Identify the preparation type.
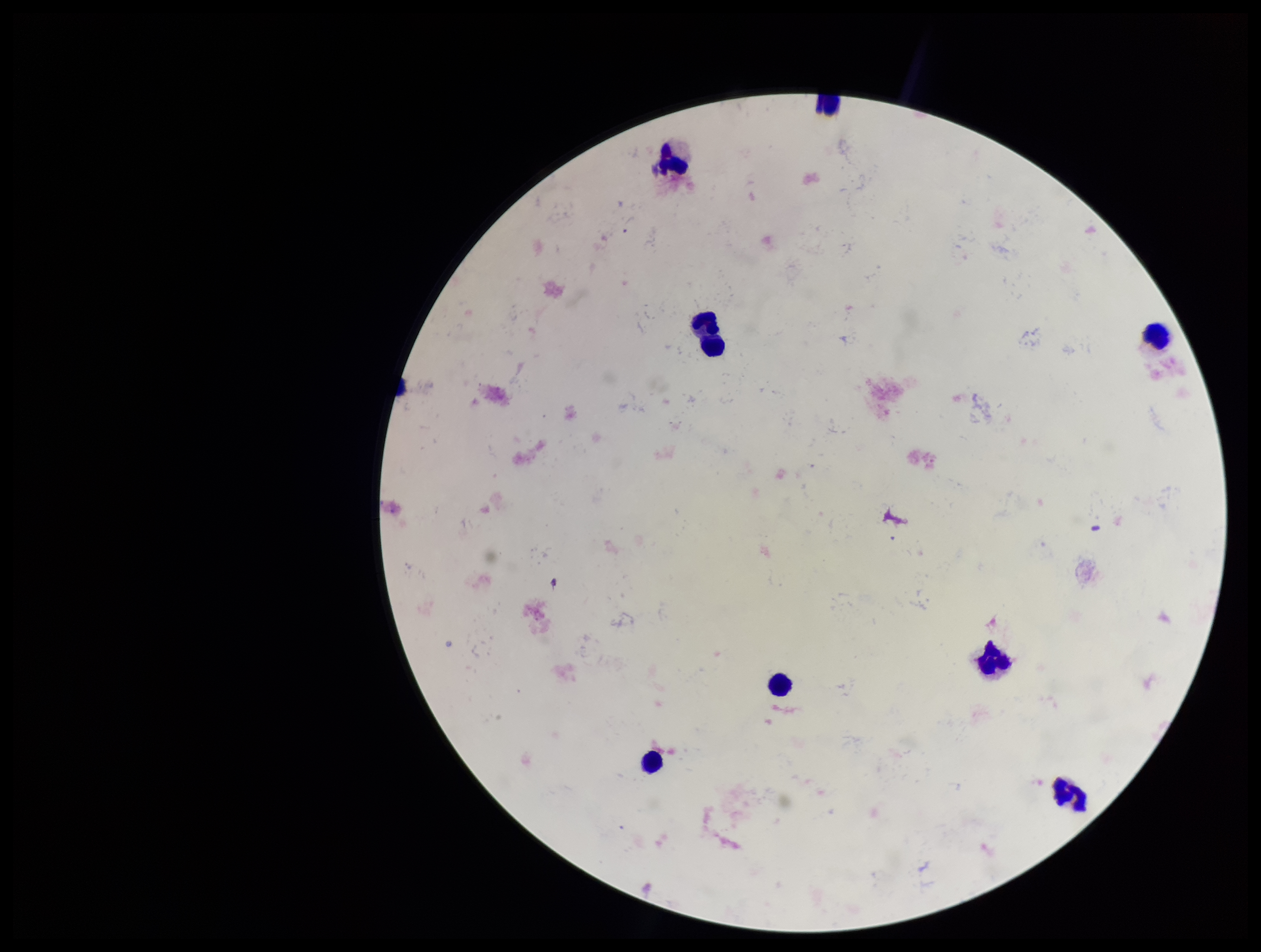
A thick smear.

{
  "image_size": "1261×952 pixels",
  "stain": "Giemsa",
  "parasite_count": 0,
  "patient_malaria_status": "negative",
  "leukocyte_count": 8,
  "plasmodium_parasites": "none identified",
  "field_of_view": "one from this slide",
  "capture": "smartphone photograph through the microscope eyepiece"
}